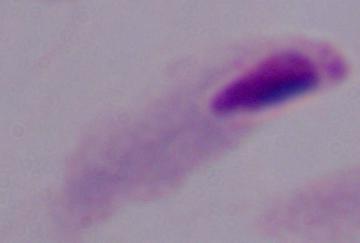
Summary:
  - Modality: micrograph
  - Identification: trichomonad
  - Magnification: 1000x